Locate every blood parasite and identify its species.
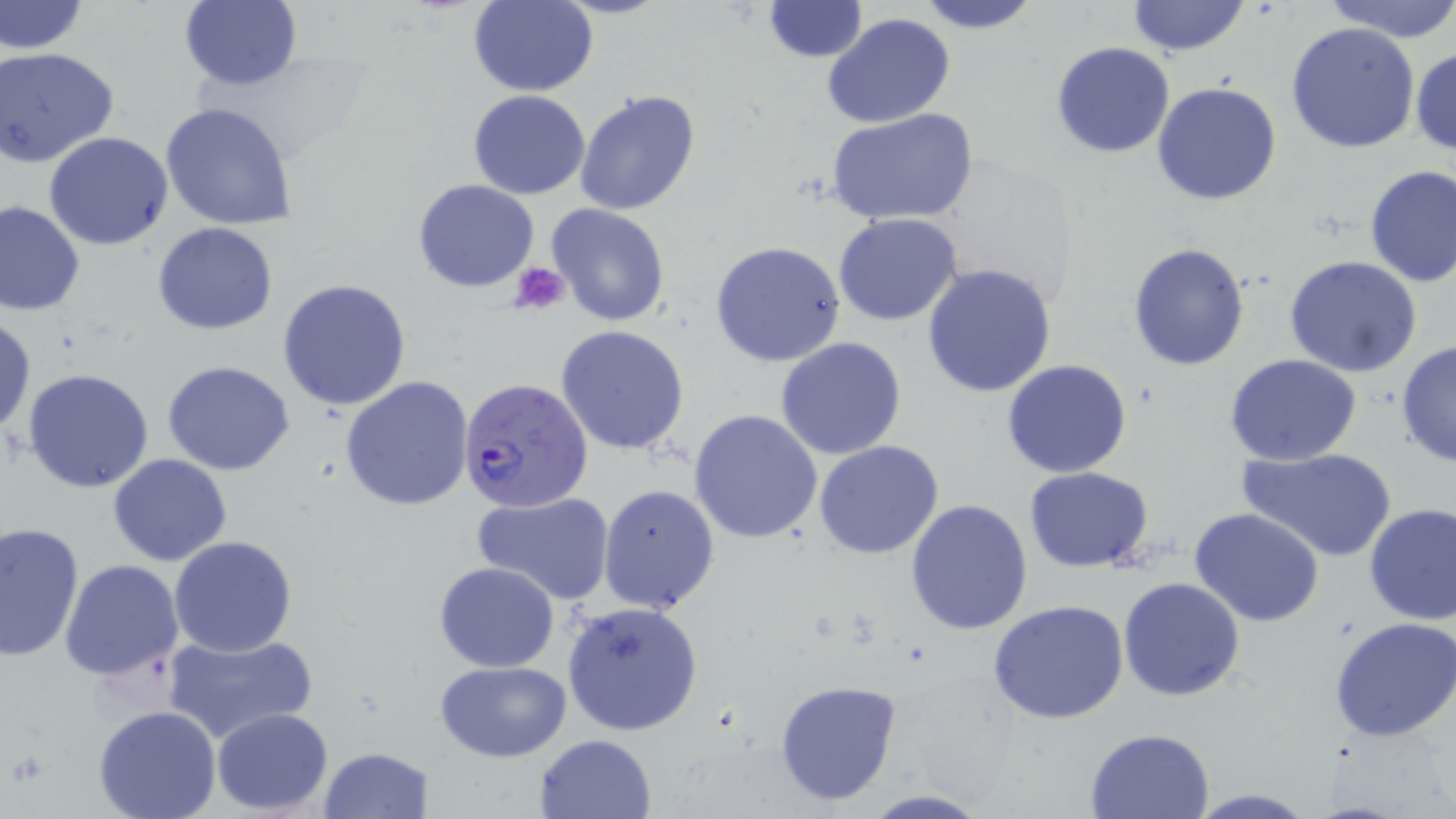

Approximate bounding boxes as named x1/y1/x2/y2 corners in pixels.
Plasmodium falciparum-infected red blood cells: (x1=460, y1=377, x2=594, y2=512).
No Plasmodium ovale, Plasmodium malariae, Plasmodium vivax, Babesia divergens, or Trypanosoma brucei observed.

Summary:
  - Uninfected red blood cell locations: (x1=467, y1=0, x2=599, y2=96), (x1=761, y1=0, x2=868, y2=62), (x1=912, y1=0, x2=1045, y2=33), (x1=1127, y1=0, x2=1252, y2=56), (x1=1324, y1=0, x2=1456, y2=41), (x1=0, y1=1, x2=88, y2=55), (x1=178, y1=1, x2=302, y2=90), (x1=823, y1=14, x2=955, y2=130), (x1=1286, y1=21, x2=1420, y2=155), (x1=1051, y1=41, x2=1176, y2=159), (x1=1410, y1=45, x2=1456, y2=157), (x1=0, y1=47, x2=120, y2=167), (x1=1152, y1=81, x2=1282, y2=206), (x1=468, y1=90, x2=591, y2=200), (x1=573, y1=91, x2=701, y2=216), (x1=160, y1=102, x2=298, y2=231), (x1=827, y1=108, x2=979, y2=227), (x1=43, y1=132, x2=172, y2=249), (x1=1362, y1=163, x2=1456, y2=289), (x1=413, y1=179, x2=540, y2=293), (x1=0, y1=201, x2=85, y2=316), (x1=546, y1=203, x2=670, y2=328), (x1=833, y1=213, x2=962, y2=327), (x1=152, y1=222, x2=278, y2=334), (x1=711, y1=240, x2=846, y2=368), (x1=1126, y1=240, x2=1251, y2=372), (x1=1285, y1=256, x2=1424, y2=376), (x1=921, y1=263, x2=1057, y2=397), (x1=278, y1=277, x2=412, y2=412), (x1=0, y1=312, x2=36, y2=439), (x1=555, y1=325, x2=690, y2=456), (x1=776, y1=336, x2=908, y2=460), (x1=1396, y1=341, x2=1455, y2=467), (x1=1224, y1=353, x2=1362, y2=465), (x1=1002, y1=358, x2=1133, y2=478), (x1=162, y1=360, x2=296, y2=475), (x1=24, y1=368, x2=154, y2=494), (x1=340, y1=375, x2=474, y2=510), (x1=689, y1=409, x2=823, y2=545), (x1=814, y1=440, x2=945, y2=558), (x1=1240, y1=446, x2=1398, y2=563), (x1=108, y1=453, x2=232, y2=566), (x1=1024, y1=467, x2=1154, y2=571), (x1=598, y1=482, x2=720, y2=615), (x1=471, y1=492, x2=616, y2=605), (x1=906, y1=498, x2=1035, y2=635), (x1=1363, y1=503, x2=1456, y2=625), (x1=1191, y1=507, x2=1325, y2=626), (x1=0, y1=521, x2=84, y2=660), (x1=169, y1=535, x2=298, y2=658), (x1=59, y1=560, x2=183, y2=682), (x1=433, y1=561, x2=561, y2=673), (x1=1118, y1=576, x2=1246, y2=701), (x1=988, y1=598, x2=1129, y2=725), (x1=561, y1=600, x2=704, y2=736), (x1=1330, y1=616, x2=1456, y2=740), (x1=163, y1=629, x2=318, y2=745), (x1=434, y1=660, x2=572, y2=762), (x1=774, y1=679, x2=904, y2=807), (x1=93, y1=704, x2=222, y2=819), (x1=212, y1=707, x2=335, y2=814), (x1=1086, y1=728, x2=1213, y2=817), (x1=534, y1=734, x2=658, y2=819), (x1=319, y1=745, x2=432, y2=817), (x1=1182, y1=790, x2=1323, y2=818)
  - Platelet locations: (x1=510, y1=262, x2=570, y2=314)
  - Slide-level diagnosis: Plasmodium falciparum
  - Image size: 1456×819 pixels
  - Modality: light microscopy
  - Stain: May-Grünwald-Giemsa
  - Magnification: 1000x
  - Field of view: one of a larger specimen
  - Preparation: thin blood smear